Report the malaria status of this cell.
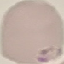
It is parasitized.

image type = automatically extracted cell patch, resized to 64 × 64 pixels
stain = Giemsa
preparation = thin blood film
capture = smartphone through the microscope eyepiece